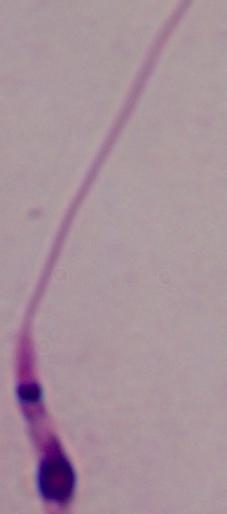
A Leishmania parasite is shown. Micrograph. Captured at 1000x magnification.